Classify this cell by malaria status.
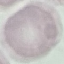

Uninfected.

Photographed with a smartphone camera at the microscope eyepiece. Automatically extracted cell patch, resized to 64 × 64 pixels. Giemsa stain. Thin blood film.